Point out leukocytes.
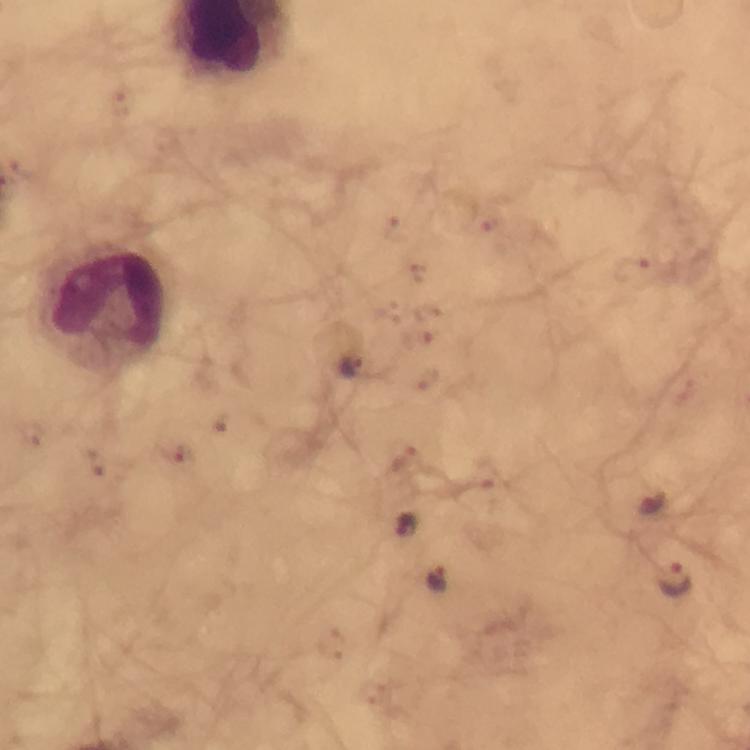
Approximate centers as {x, y} in pixels.
Leukocytes: {106, 307}.

Plasmodium parasite locations: {491, 220}, {395, 228}, {634, 269}, {417, 273}, {426, 311}, {420, 339}, {353, 366}, {222, 425}, {32, 433}, {404, 458}, {173, 460}, {94, 465}, {650, 504}, {405, 524}, {438, 579}, {675, 579}, {334, 644}. From a diagnostic examination for malaria. Giemsa-stained preparation. Image is 750×750 pixels. At 100x magnification. A crop from one field of view. Smartphone photograph taken through a microscope. Thick blood smear. Immersion oil applied.